Comment on the background quality.
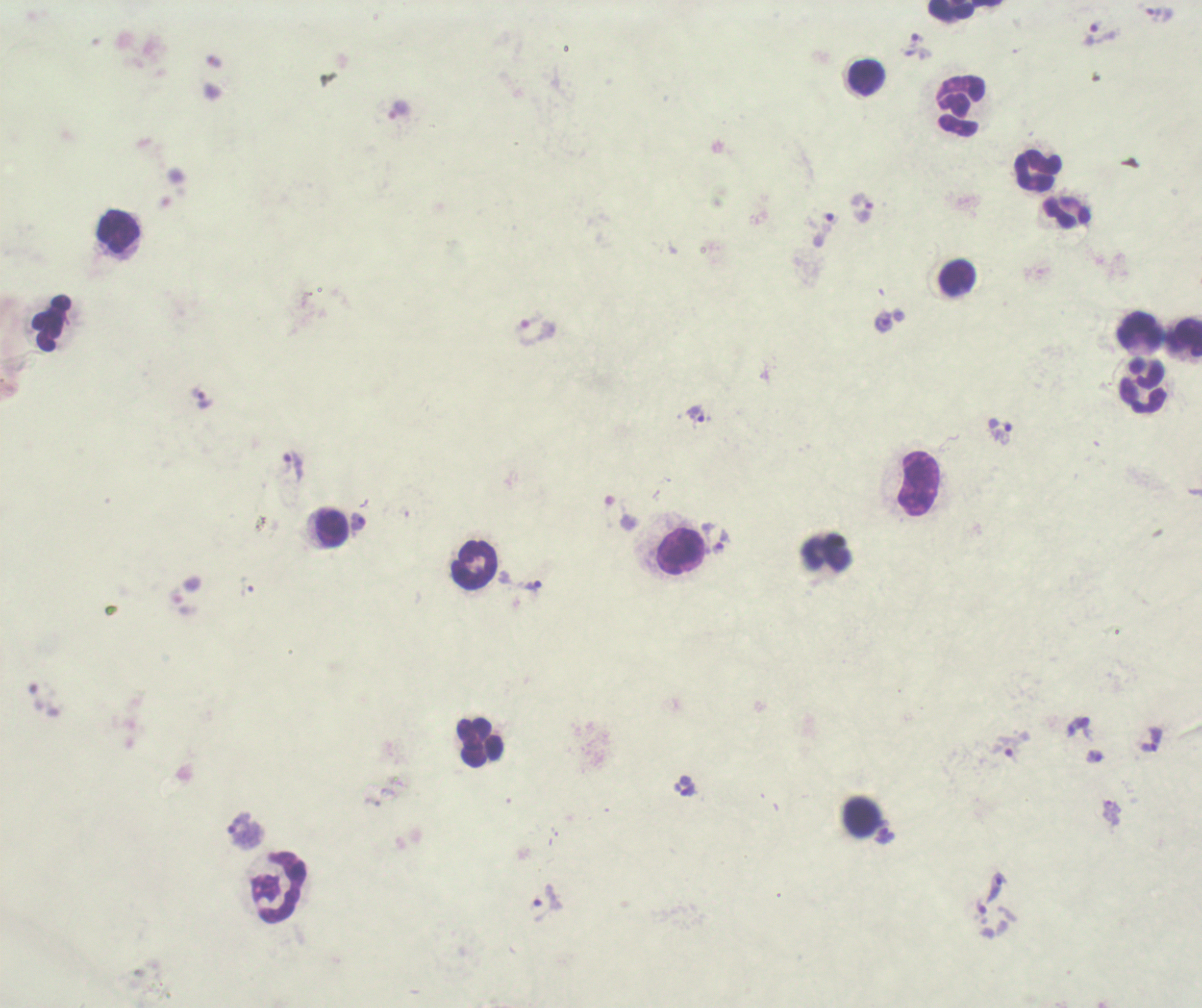

It is poor.

coordinate format = approximate centers as {x, y} in pixels
trophozoite locations = {1154, 14}, {1091, 35}, {916, 39}, {398, 110}, {861, 203}, {830, 221}, {885, 322}, {534, 329}, {202, 399}, {696, 414}, {1004, 433}, {292, 465}, {358, 523}, {720, 541}, {533, 585}, {1152, 739}, {1008, 746}, {1094, 756}, {685, 786}, {1111, 812}, {245, 829}, {885, 835}, {996, 889}, {547, 902}, {982, 907}
leukocyte locations = {951, 11}, {867, 78}, {960, 106}, {1037, 171}, {1067, 212}, {118, 231}, {958, 278}, {51, 322}, {1139, 331}, {1186, 337}, {1143, 386}, {919, 483}, {332, 529}, {682, 552}, {826, 555}, {475, 564}, {479, 742}, {862, 816}, {278, 886}
image size = 1202×1008 pixels
coloration quality = bad
stain = Romanowsky
field of view = single
magnification = 100x
context = previously used in an actual diagnosis
result = Plasmodium parasites detected
preparation = thick blood film